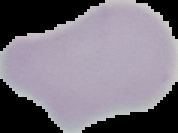

Summary:
  - Image size: 178×133 pixels
  - Preparation: thin blood film
  - Image type: cell region segmented out of the field of view; surrounding area masked to black
  - Result: no malaria parasites detected